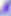 Photomicrograph. Toxoplasma gondii is seen. 400x magnification.